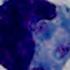
Micrograph. A leukocyte is seen. Captured at 1000x magnification.